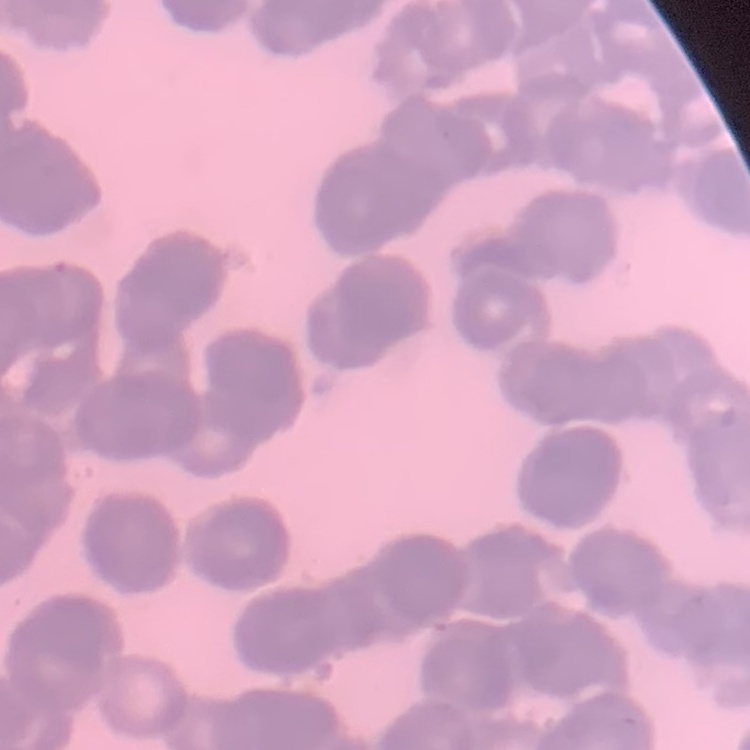
{
  "erythrocyte_morphology": "rouleaux formation",
  "preparation": "thin blood smear",
  "stain": "Field's or Giemsa",
  "image_type": "square crop of a larger photomicrograph"
}